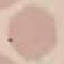
Malaria status: uninfected. Giemsa stain. Cell patch, automatically extracted from a larger field of view and resized to 64 × 64 pixels. Thin blood smear. Acquired by smartphone through the microscope eyepiece.